Outline each blood parasite and name the species.
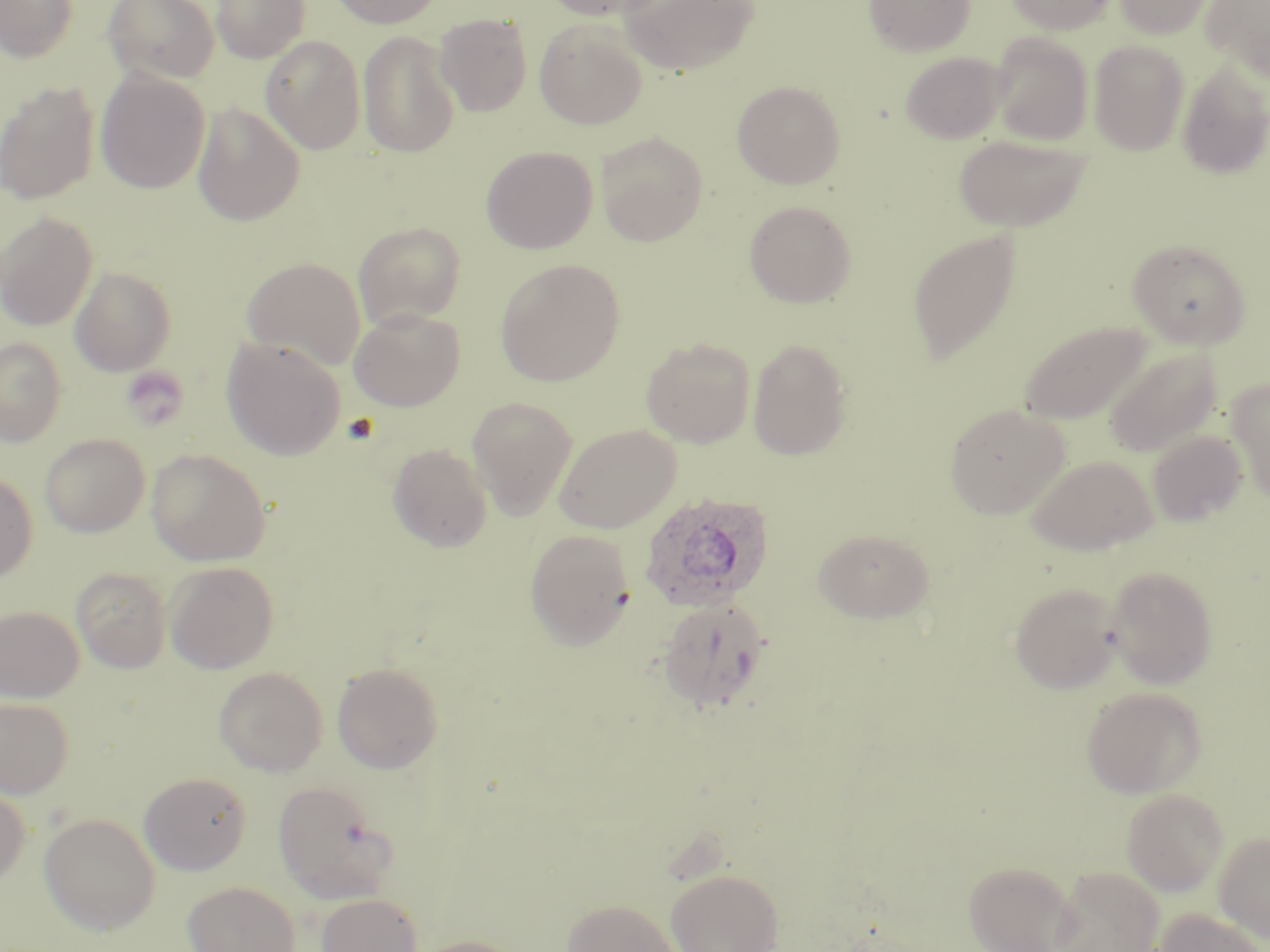

Approximate bounding boxes as (x1, y1, x2, y2) in pixels.
Plasmodium ovale-infected red blood cells: (638, 491, 774, 613).
No Plasmodium falciparum, Plasmodium malariae, Plasmodium vivax, Babesia divergens, or Trypanosoma brucei observed.

slide-level diagnosis = Plasmodium ovale
image size = 1270×952 pixels
magnification = 1000x
stain = May-Grünwald-Giemsa
modality = optical microscopy
preparation = thin blood smear
field of view = single
uninfected red blood cell locations = approximate bounding boxes as (x1, y1, x2, y2) in pixels: (0, 0, 78, 63), (103, 0, 219, 84), (211, 0, 310, 63), (330, 0, 445, 29), (541, 0, 670, 21), (619, 0, 760, 75), (864, 0, 974, 57), (1004, 0, 1117, 34), (1113, 0, 1216, 39), (1200, 0, 1270, 81), (434, 13, 534, 116), (534, 19, 648, 129), (357, 30, 460, 158), (990, 33, 1094, 145), (260, 35, 366, 154), (1087, 40, 1189, 155), (899, 51, 1006, 145), (1177, 60, 1270, 180), (96, 69, 211, 193), (0, 80, 101, 205), (732, 80, 846, 189), (193, 103, 305, 225), (595, 131, 708, 246), (952, 133, 1093, 232), (481, 146, 598, 254), (744, 200, 857, 308), (0, 212, 98, 331), (353, 221, 466, 329), (907, 229, 1022, 365), (1127, 239, 1251, 349), (241, 257, 365, 370), (496, 259, 625, 386), (70, 265, 176, 376), (349, 307, 465, 411), (1019, 320, 1154, 425), (0, 337, 66, 446), (221, 337, 346, 460), (641, 337, 756, 448), (747, 338, 853, 461), (1103, 347, 1222, 459), (1226, 379, 1270, 503), (467, 397, 578, 520), (944, 402, 1070, 519), (554, 424, 681, 533), (1147, 430, 1247, 526), (39, 433, 150, 537), (387, 442, 493, 552), (146, 449, 270, 565), (1024, 453, 1158, 555), (0, 471, 37, 584), (813, 528, 935, 623), (525, 529, 635, 650), (165, 561, 278, 674), (1104, 565, 1218, 689), (71, 567, 171, 673), (1008, 582, 1124, 694), (657, 598, 770, 715), (0, 605, 84, 702), (331, 662, 444, 774), (214, 666, 328, 776), (1080, 686, 1207, 799), (0, 697, 73, 799), (138, 771, 251, 874), (274, 781, 399, 904), (0, 785, 30, 886), (1121, 789, 1228, 896), (39, 813, 160, 935), (1214, 830, 1270, 942), (963, 861, 1077, 952), (1050, 866, 1165, 952), (666, 868, 784, 952), (183, 881, 300, 952), (316, 893, 423, 952), (561, 899, 679, 952), (1153, 909, 1267, 952), (413, 936, 524, 952)